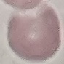

Result: no malaria parasites seen. Photographed with a smartphone camera at the microscope eyepiece. Giemsa stain. Cell patch, automatically extracted from a larger field of view and resized to 64 × 64 pixels. Thin blood film.